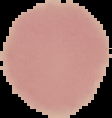
image size = 112×118 pixels
preparation = thin blood smear
result = no malaria parasites detected
image type = segmented cell region on a black background